Name the parasite shown.
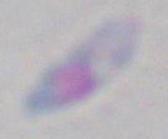

Toxoplasma gondii.

Micrograph. Captured at 1000x magnification.